Describe the morphology of the erythrocytes.
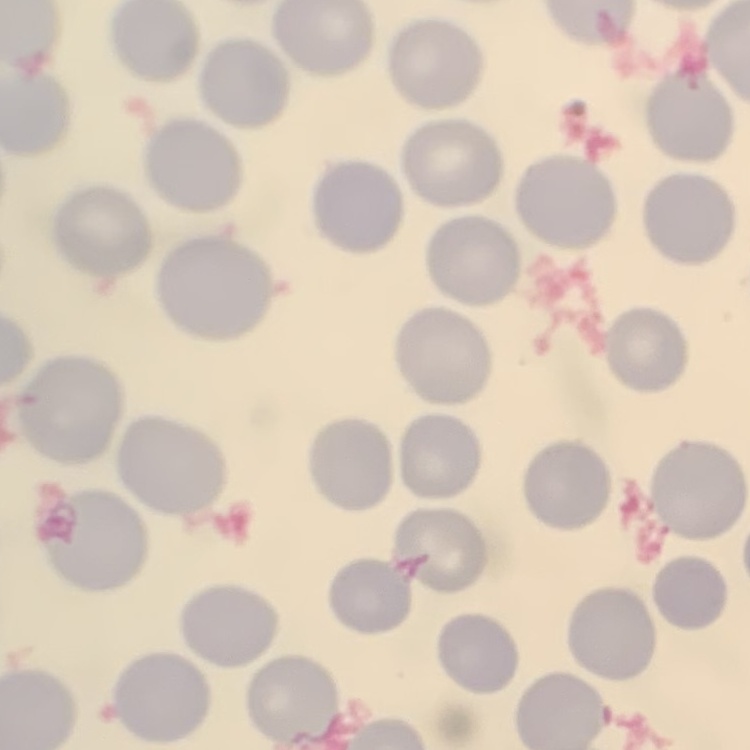
No rouleaux formation.

Stained with either Field's or Giemsa. Thin peripheral smear. One tile cut from a larger photomicrograph.